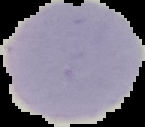
Summary:
  - Image type: segmented cell region with the area outside set to black
  - Malaria status: uninfected
  - Preparation: thin blood smear
  - Image size: 145×127 pixels